State which parasite is depicted.
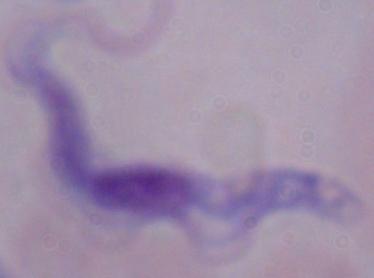
This is a trypanosome.

Summary:
  - Modality: micrograph
  - Magnification: 1000x